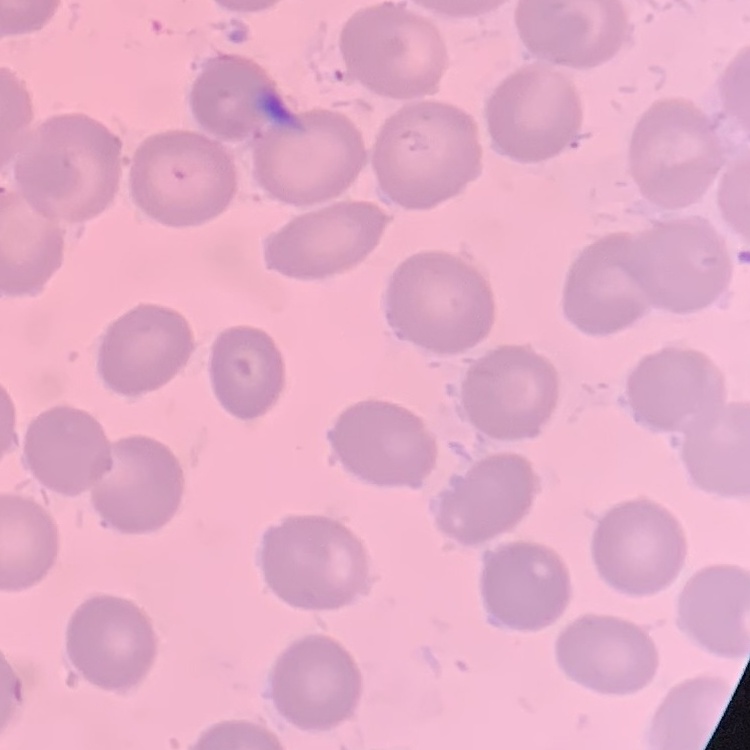

Summary:
  - Red blood cell morphology: no rouleaux formation
  - Stain: Field's or Giemsa
  - Image type: square crop of a larger photomicrograph
  - Preparation: thin blood film